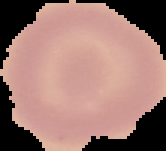

Summary:
  - Image size: 166×151 pixels
  - Malaria status: uninfected
  - Image type: segmented cell region with the area outside set to black
  - Preparation: thin blood film